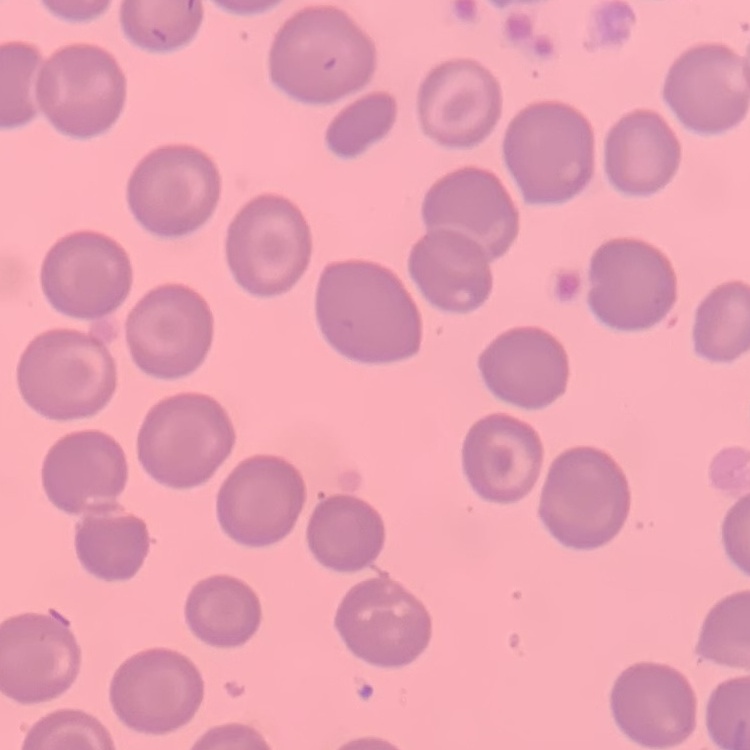

erythrocyte_morphology: no rouleaux formation
stain: Field's or Giemsa
image_type: square crop of a larger photomicrograph
preparation: thin blood film